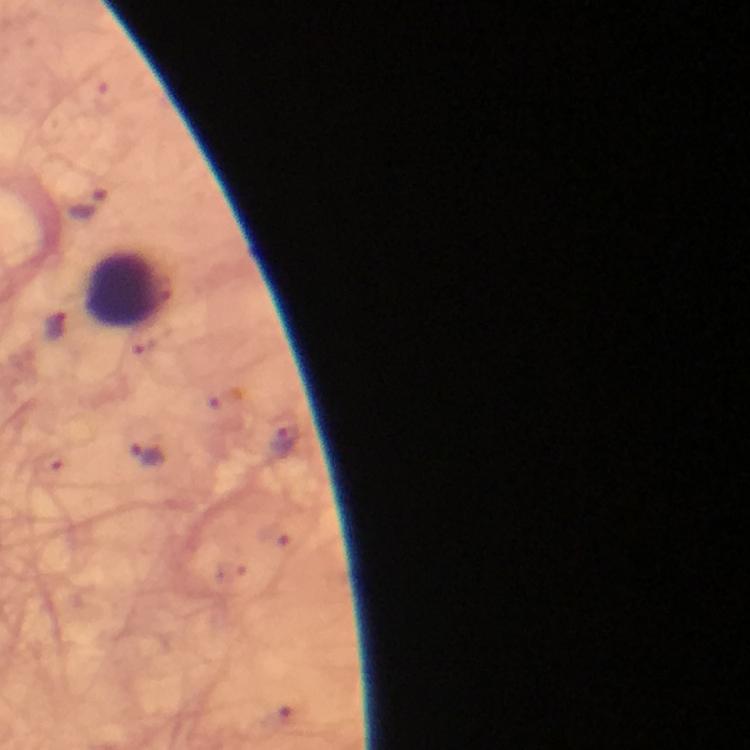
Approximate centers as {x, y} in pixels.
Summary:
  - Plasmodium parasite locations: {92, 204}, {56, 325}, {148, 453}
  - Leukocyte locations: {129, 289}
  - Context: from a diagnostic examination for malaria
  - Image size: 750×750 pixels
  - Preparation: thick smear
  - Immersion oil: applied
  - Capture: smartphone photograph through a microscope
  - Magnification: 100x
  - Stain: Giemsa
  - Cropped from: one field of view